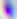

{
  "identification": "Toxoplasma gondii",
  "magnification": "400x",
  "modality": "photomicrograph"
}